Outline every leukocyte.
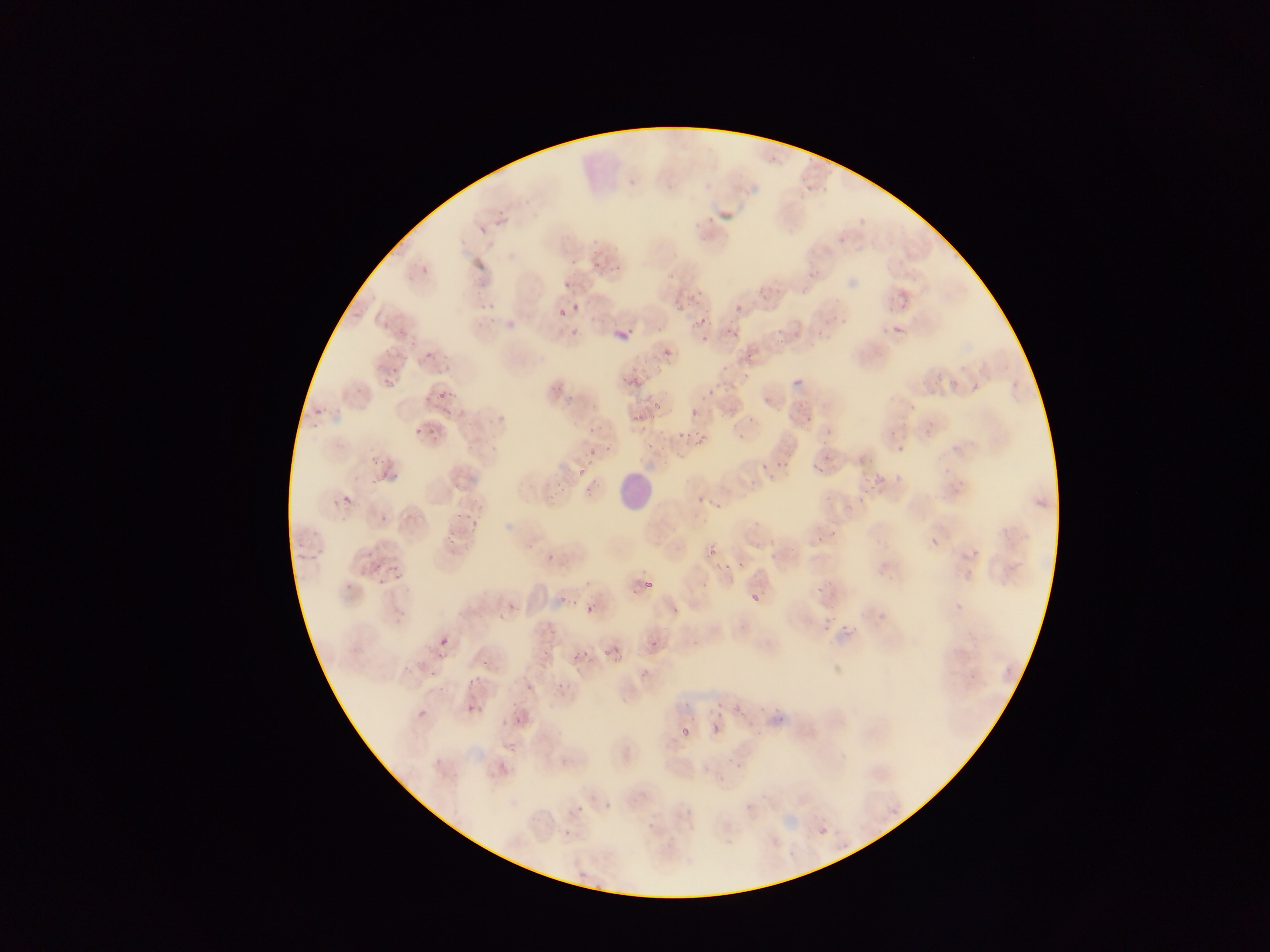

Approximate bounding boxes as [left, top, right, bottom] in pixels.
Leukocytes: [618, 471, 656, 512].

capture = mobile-phone photograph through a microscope
Plasmodium parasite locations = approximate bounding boxes as [left, top, right, bottom] in pixels: [613, 263, 621, 272], [564, 281, 571, 289], [733, 300, 744, 310], [573, 302, 581, 311], [558, 308, 565, 317], [699, 315, 711, 328], [720, 319, 734, 333], [891, 324, 904, 335], [884, 325, 894, 335], [621, 327, 637, 331], [663, 348, 672, 357], [423, 352, 434, 362], [382, 359, 394, 386], [792, 366, 808, 388], [437, 380, 455, 405], [304, 388, 326, 420], [704, 389, 715, 401], [412, 409, 432, 437], [690, 409, 698, 418], [802, 414, 815, 424], [687, 422, 709, 455], [671, 428, 684, 444], [889, 430, 897, 438], [897, 445, 905, 454], [588, 447, 595, 458], [771, 451, 794, 468], [757, 453, 777, 470], [810, 457, 828, 475], [374, 460, 399, 492], [895, 474, 904, 484], [876, 475, 885, 484], [864, 480, 877, 506], [692, 485, 709, 504], [341, 494, 352, 505], [454, 509, 468, 530], [380, 514, 389, 523], [464, 524, 475, 535], [930, 538, 939, 547], [769, 540, 776, 549], [707, 547, 715, 555], [373, 549, 411, 584], [541, 550, 565, 561], [738, 560, 745, 570], [645, 581, 654, 589], [554, 591, 568, 605], [750, 593, 759, 601], [585, 604, 595, 613], [671, 606, 680, 615], [823, 625, 832, 634], [439, 637, 448, 646], [649, 639, 657, 648], [602, 646, 616, 656], [571, 647, 586, 661], [469, 677, 477, 685], [552, 680, 567, 694], [467, 704, 476, 713], [733, 706, 747, 716], [713, 723, 723, 734], [680, 728, 689, 738], [576, 806, 585, 814], [819, 828, 827, 835], [563, 829, 570, 838] | approximate [x, y] pixel centers of objects too small to bound: [704, 338]
preparation = thin blood smear
country = Ghana
image size = 1270×952 pixels
field of view = single